Locate and identify every blood parasite.
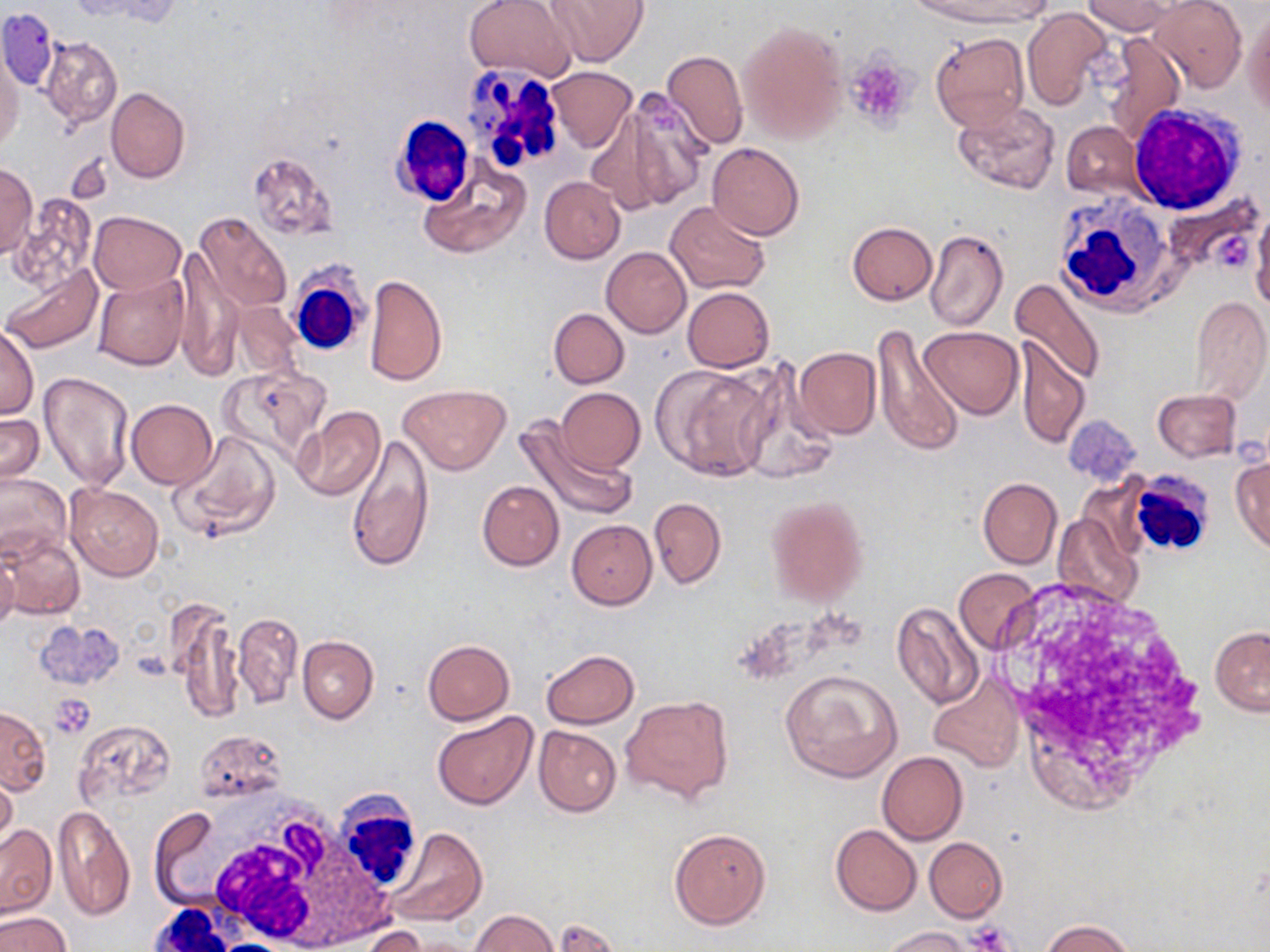

No blood parasites seen.

Approximate bounding boxes as (x1,y1)-(x2,y2) corner pairs in pixels. White blood cell locations: (458,60)-(571,181), (1129,105)-(1248,214), (387,116)-(472,204), (1053,194)-(1180,313), (288,269)-(371,357), (1124,469)-(1217,559), (327,786)-(425,896), (185,796)-(373,949), (145,904)-(250,950). Uninfected red blood cell locations: (465,0)-(575,83), (541,0)-(650,67), (910,0)-(1052,27), (1082,0)-(1174,35), (1150,0)-(1247,92), (74,1)-(184,28), (1022,7)-(1113,110), (1244,7)-(1270,116), (1,9)-(59,93), (738,18)-(848,146), (929,32)-(1030,133), (1102,32)-(1186,143), (41,36)-(122,129), (660,49)-(749,152), (0,53)-(23,156), (546,67)-(636,152), (106,87)-(189,183), (617,90)-(711,210), (953,101)-(1061,195), (586,104)-(675,218), (1061,122)-(1143,198), (707,142)-(805,241), (246,150)-(339,242), (0,162)-(37,257), (417,162)-(531,260), (540,176)-(626,263), (12,196)-(97,292), (665,200)-(772,295), (1252,209)-(1270,313), (88,211)-(186,294), (195,213)-(292,314), (847,222)-(937,305), (925,229)-(1008,331), (174,246)-(241,381), (602,246)-(691,337), (2,262)-(102,355), (92,274)-(189,371), (364,274)-(447,387), (1008,277)-(1104,385), (683,287)-(774,372), (1190,296)-(1270,403), (232,300)-(303,379), (549,308)-(629,387), (869,324)-(965,456), (0,326)-(39,418), (919,326)-(1025,420), (1015,338)-(1089,449), (794,347)-(880,439), (654,363)-(774,481), (736,364)-(837,484), (217,365)-(330,464), (38,373)-(136,491), (398,385)-(511,475), (556,387)-(646,474), (1153,390)-(1241,462), (125,399)-(217,488), (291,406)-(386,502), (0,412)-(44,486), (514,417)-(635,522), (171,429)-(283,543), (345,434)-(435,574), (1231,455)-(1270,553), (0,472)-(70,561), (978,478)-(1062,568), (477,480)-(565,570), (64,484)-(164,582), (765,495)-(869,605), (649,497)-(726,588), (1053,512)-(1142,609), (567,519)-(657,610), (1,533)-(84,621), (0,550)-(19,635), (954,567)-(1041,655), (166,599)-(243,726), (891,603)-(984,709), (232,612)-(303,710), (1210,626)-(1269,716), (298,635)-(378,723), (422,638)-(514,724), (541,650)-(640,729), (779,669)-(903,781), (929,680)-(1023,773), (620,696)-(733,804), (1,706)-(50,794), (431,712)-(538,809), (72,720)-(174,810), (534,725)-(621,817), (192,729)-(286,803), (878,751)-(968,845), (0,770)-(18,852), (52,805)-(135,921), (148,809)-(220,896), (831,823)-(921,915), (0,824)-(56,916), (669,827)-(771,930), (390,828)-(486,926), (925,837)-(1006,922), (470,910)-(557,952), (0,911)-(71,952), (1040,920)-(1137,952), (881,926)-(973,952), (362,927)-(429,952). Platelet locations: (844,54)-(916,132), (1217,231)-(1257,273), (50,695)-(96,738), (556,919)-(617,952), (968,923)-(1015,951). Slide-level diagnosis: negative for blood parasites. 1000x magnification. One field of a larger specimen. May-Grünwald-Giemsa-stained preparation. Image is 1270×952 pixels. Light microscopy. Thin blood smear.